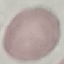
result = no malaria parasites seen
preparation = thin smear
capture = smartphone camera at the microscope eyepiece
stain = Giemsa
image type = cell patch, automatically extracted from a larger field of view and resized to 64 × 64 pixels